Assess this cell for malaria.
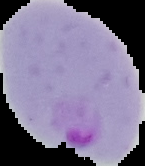
Parasitized.

From a thin blood film. Image is 145×166 pixels. Cell region segmented out of the field of view; the surrounding area is masked to black.